Assess this cell for malaria.
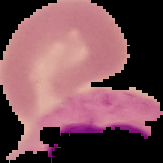
Uninfected.

Image is 163×163 pixels. From a thin blood film. The area outside the segmented cell region is set to black.